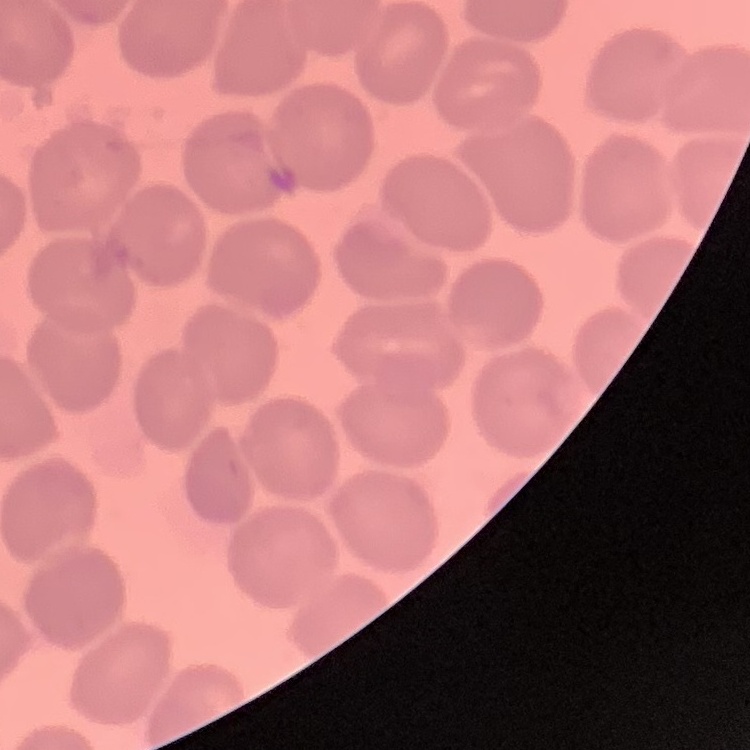
The erythrocytes exhibit no rouleaux formation. Thin blood smear. Field's or Giemsa stain. One tile cut from a larger photomicrograph.